Identify the parasite.
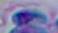

This is Toxoplasma gondii.

Summary:
  - Modality: micrograph
  - Magnification: 1000x